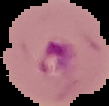

preparation = thin blood smear
image size = 109×106 pixels
image type = segmented cell region on a black background
result = malaria parasites detected